Assess this cell for malaria.
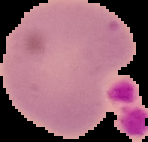
Uninfected.

The area outside the segmented cell region is set to black. Image is 148×142 pixels. From a thin blood film.